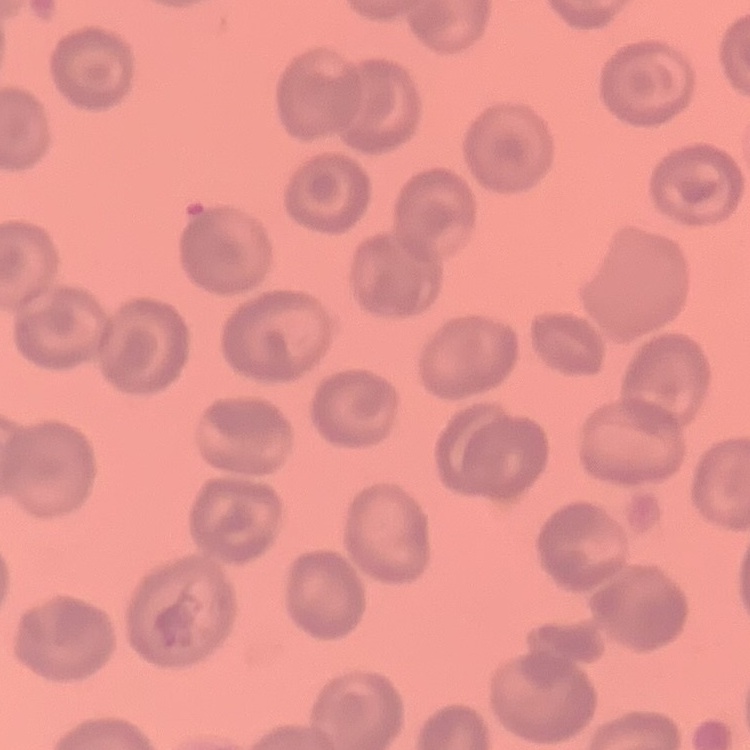
{
  "erythrocyte_morphology": "no rouleaux formation",
  "image_type": "one tile cut from a larger photomicrograph",
  "stain": "Field's or Giemsa",
  "preparation": "thin blood smear"
}